Assess the morphology of the red blood cells.
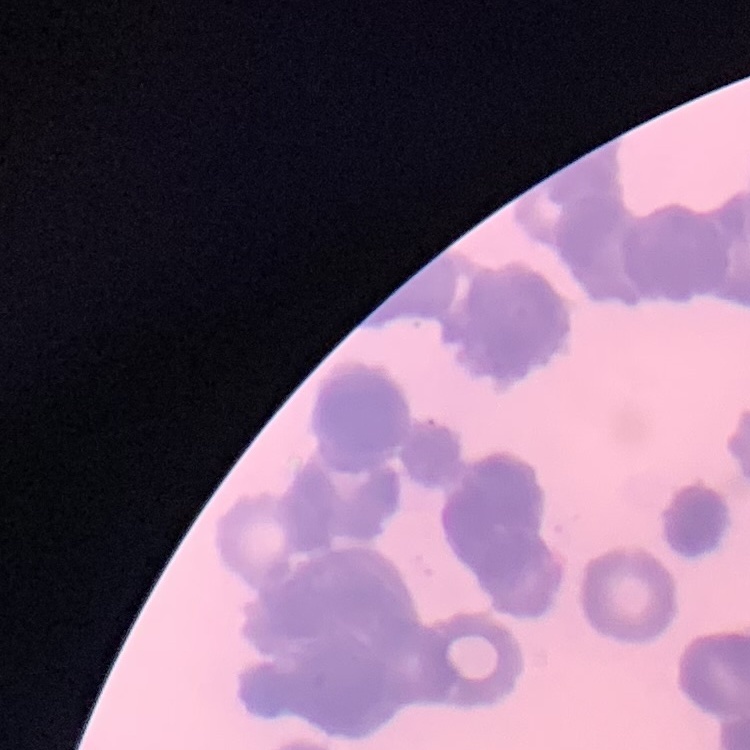
Rouleaux formation.

One tile cut from a larger photomicrograph. Thin peripheral smear. Field's or Giemsa stain.